Classify this cell by malaria status.
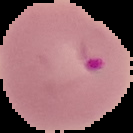

It is parasitized.

Image is 133×133 pixels. From a thin blood film. Segmented cell region on a black background.